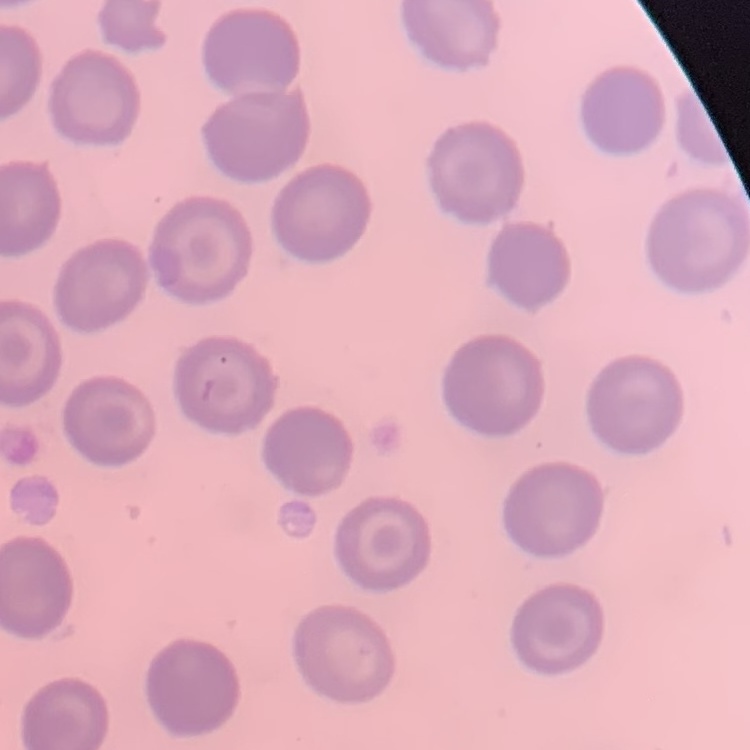
red_blood_cell_morphology: no rouleaux formation
stain: Field's or Giemsa
preparation: thin blood film
image_type: one tile cut from a larger photomicrograph